Report the malaria status of this cell.
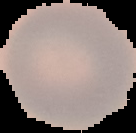

Uninfected.

image size = 136×133 pixels
image type = segmented cell region on a black background
preparation = thin blood film